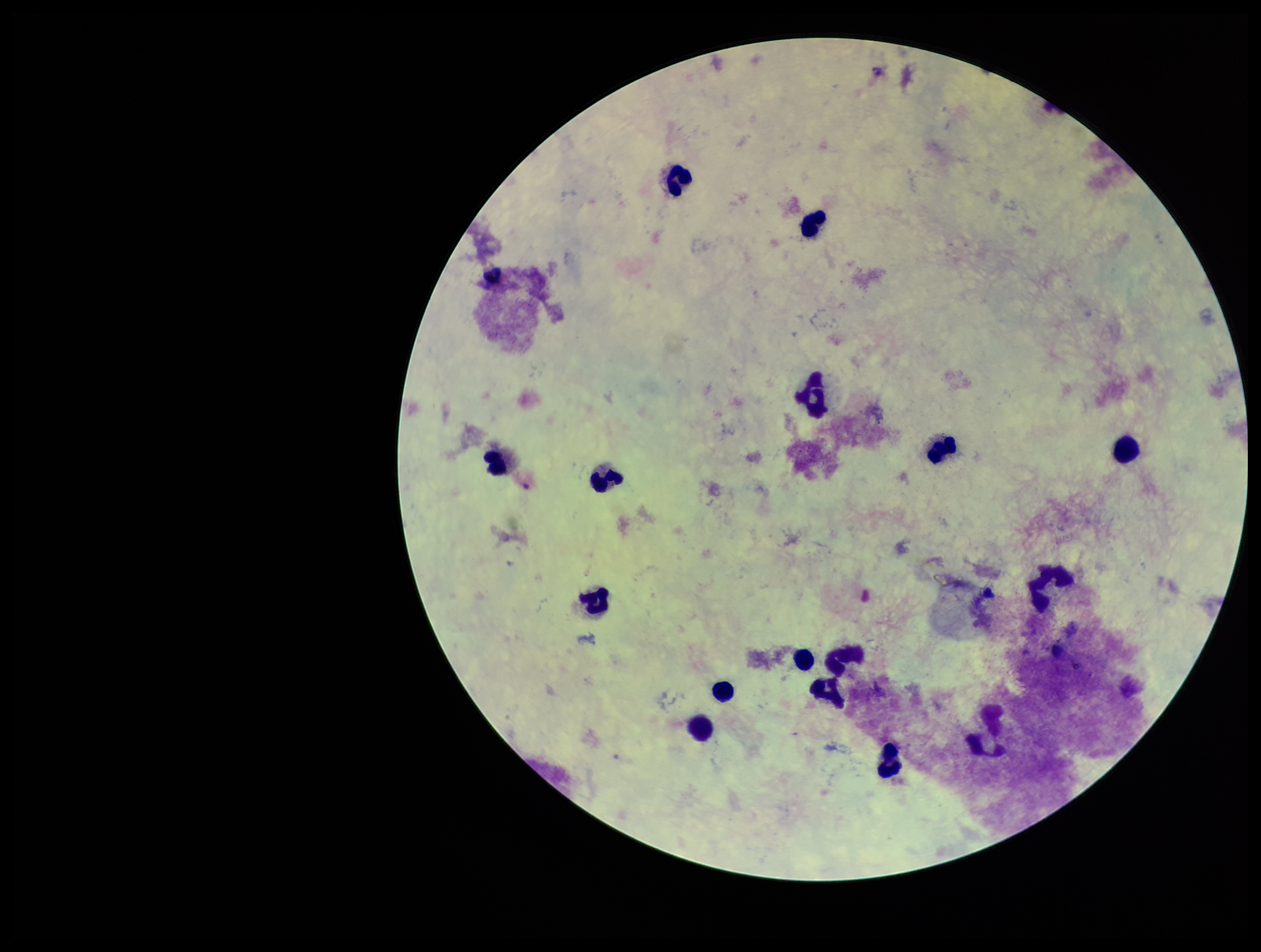

Plasmodium parasites: none detected. Parasite count: 0. Single field of view. Preparation: thick smear. Stained with Giemsa. Leukocyte count: 15. Photographed through the microscope eyepiece with a smartphone camera. Image is 1261×952 pixels. Patient malaria status: negative.